State which parasite is depicted.
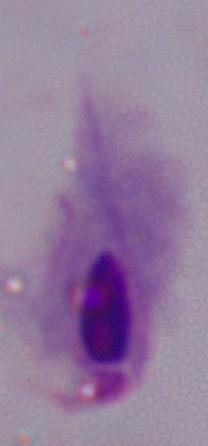
This is a trichomonad.

Micrograph. 1000x magnification.